Assess this cell for malaria.
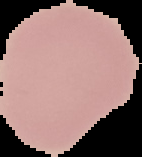
It is uninfected.

From a thin blood smear. Image is 142×157 pixels. The area outside the segmented cell region is set to black.